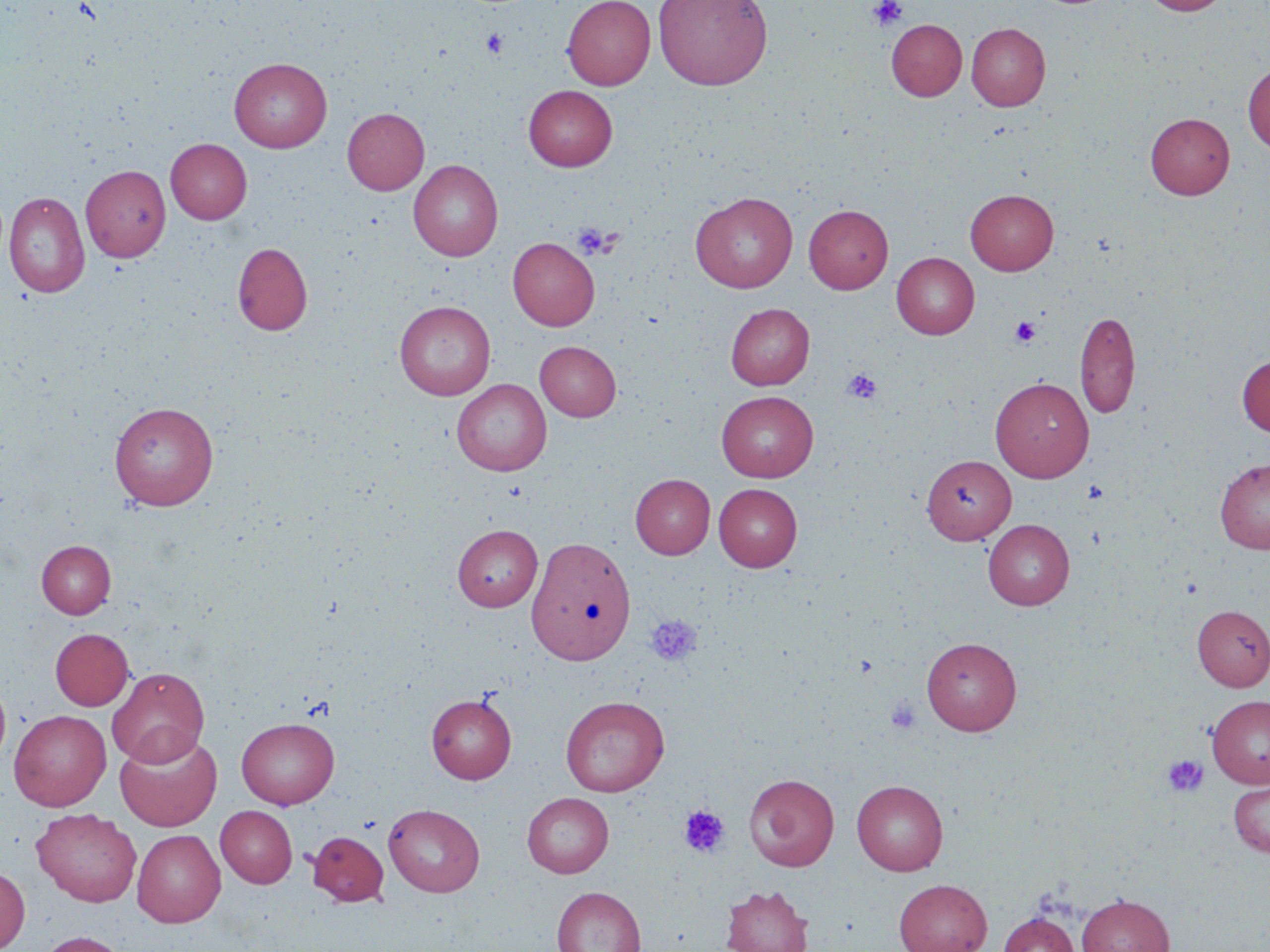

Approximate bounding boxes as named x1/y1/x2/y2 corners in pixels. Platelet locations: (x1=868, y1=0, x2=907, y2=32), (x1=481, y1=28, x2=509, y2=58), (x1=572, y1=223, x2=617, y2=259), (x1=1010, y1=316, x2=1041, y2=346), (x1=842, y1=369, x2=882, y2=404), (x1=644, y1=614, x2=702, y2=667), (x1=886, y1=697, x2=921, y2=733), (x1=1162, y1=755, x2=1208, y2=798), (x1=679, y1=804, x2=730, y2=857). Uninfected red blood cell locations: (x1=562, y1=0, x2=655, y2=89), (x1=653, y1=0, x2=773, y2=90), (x1=1141, y1=0, x2=1229, y2=16), (x1=886, y1=19, x2=967, y2=101), (x1=966, y1=23, x2=1050, y2=111), (x1=230, y1=58, x2=332, y2=152), (x1=1243, y1=63, x2=1270, y2=153), (x1=523, y1=85, x2=617, y2=171), (x1=342, y1=108, x2=429, y2=194), (x1=1145, y1=112, x2=1235, y2=199), (x1=166, y1=138, x2=252, y2=224), (x1=408, y1=160, x2=503, y2=261), (x1=81, y1=165, x2=170, y2=262), (x1=965, y1=189, x2=1059, y2=275), (x1=4, y1=191, x2=90, y2=297), (x1=690, y1=191, x2=798, y2=293), (x1=804, y1=204, x2=893, y2=294), (x1=508, y1=237, x2=599, y2=330), (x1=232, y1=242, x2=313, y2=336), (x1=892, y1=252, x2=979, y2=339), (x1=394, y1=301, x2=494, y2=399), (x1=725, y1=303, x2=814, y2=390), (x1=1075, y1=309, x2=1140, y2=419), (x1=535, y1=341, x2=621, y2=421), (x1=1237, y1=355, x2=1270, y2=437), (x1=990, y1=377, x2=1094, y2=482), (x1=452, y1=379, x2=551, y2=476), (x1=716, y1=391, x2=818, y2=482), (x1=109, y1=401, x2=219, y2=510), (x1=923, y1=455, x2=1016, y2=544), (x1=1215, y1=458, x2=1270, y2=554), (x1=630, y1=474, x2=715, y2=559), (x1=714, y1=483, x2=802, y2=571), (x1=983, y1=519, x2=1075, y2=610), (x1=452, y1=524, x2=542, y2=611), (x1=527, y1=535, x2=636, y2=665), (x1=36, y1=540, x2=116, y2=618), (x1=1192, y1=605, x2=1270, y2=690), (x1=50, y1=628, x2=134, y2=710), (x1=922, y1=637, x2=1021, y2=735), (x1=107, y1=667, x2=209, y2=767), (x1=0, y1=677, x2=11, y2=771), (x1=426, y1=693, x2=517, y2=784), (x1=1206, y1=695, x2=1270, y2=788), (x1=560, y1=696, x2=669, y2=796), (x1=9, y1=709, x2=111, y2=810), (x1=236, y1=718, x2=339, y2=809), (x1=115, y1=730, x2=222, y2=831), (x1=744, y1=773, x2=839, y2=871), (x1=1228, y1=779, x2=1270, y2=857), (x1=852, y1=780, x2=948, y2=876), (x1=522, y1=792, x2=613, y2=878), (x1=384, y1=804, x2=485, y2=897), (x1=216, y1=806, x2=297, y2=888), (x1=31, y1=808, x2=141, y2=907), (x1=132, y1=829, x2=225, y2=927), (x1=308, y1=831, x2=389, y2=906), (x1=0, y1=866, x2=30, y2=952), (x1=893, y1=878, x2=992, y2=952), (x1=720, y1=884, x2=814, y2=952), (x1=552, y1=887, x2=646, y2=952), (x1=1076, y1=893, x2=1174, y2=952), (x1=999, y1=912, x2=1079, y2=952), (x1=34, y1=930, x2=131, y2=952). Slide-level diagnosis: no evidence of blood parasites. One field of a larger specimen. May-Grünwald-Giemsa-stained preparation. 1000x magnification. Optical microscopy. Image is 1270×952 pixels. Thin blood film.